Assess for parasitized red blood cells.
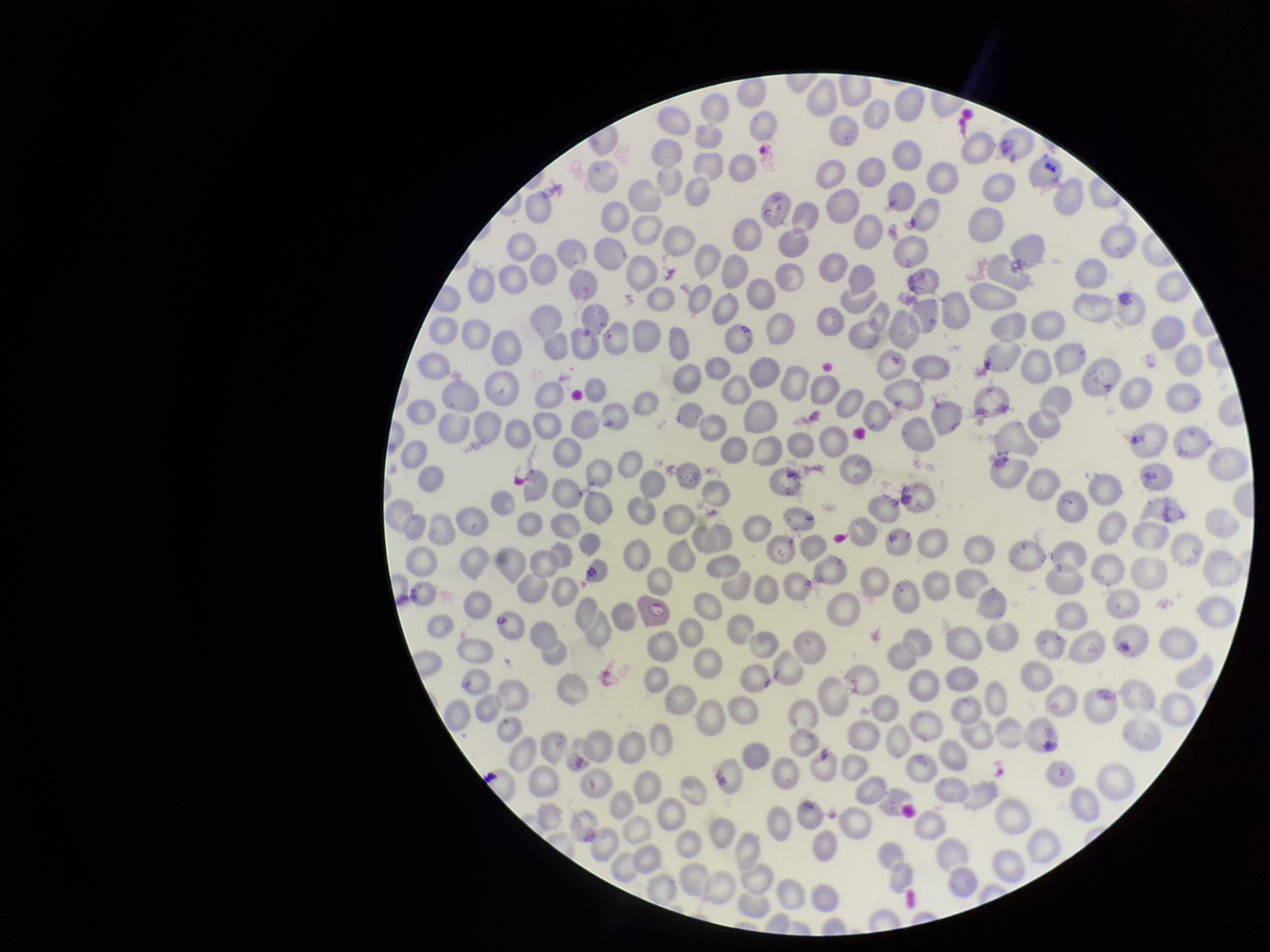

Detected.

{
  "species_reported_for_this_patient": "Plasmodium falciparum",
  "image_size": "1270×952 pixels",
  "red_blood_cell_count": 289,
  "preparation": "thin smear",
  "capture": "smartphone photograph through the microscope eyepiece",
  "patient_malaria_status": "positive",
  "parasitized_red_blood_cell_count": 1,
  "stain": "Giemsa",
  "field_of_view": "single"
}